Describe the morphology of the erythrocytes.
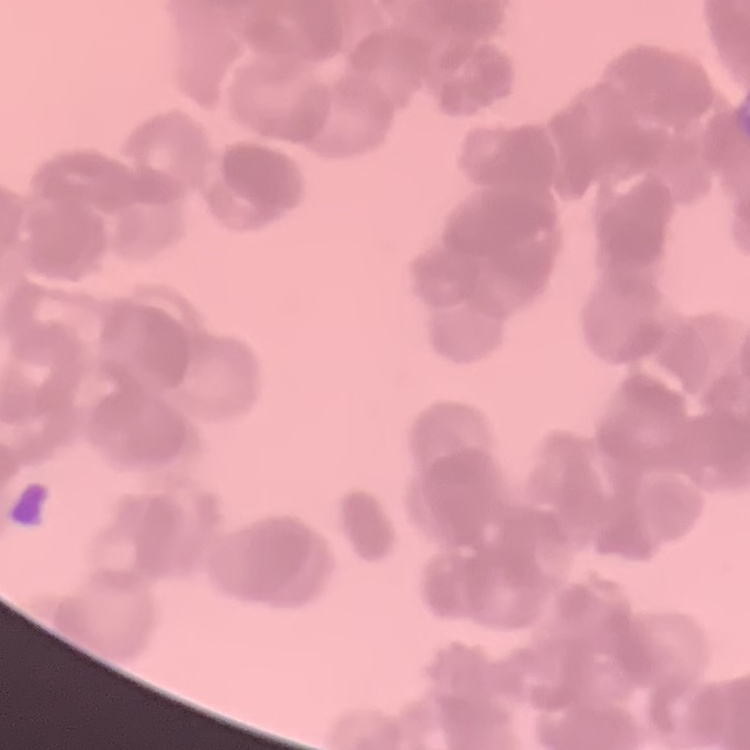
Rouleaux formation.

One tile cut from a larger photomicrograph. Field's or Giemsa stain. Thin peripheral smear.